Describe the morphology of the erythrocytes.
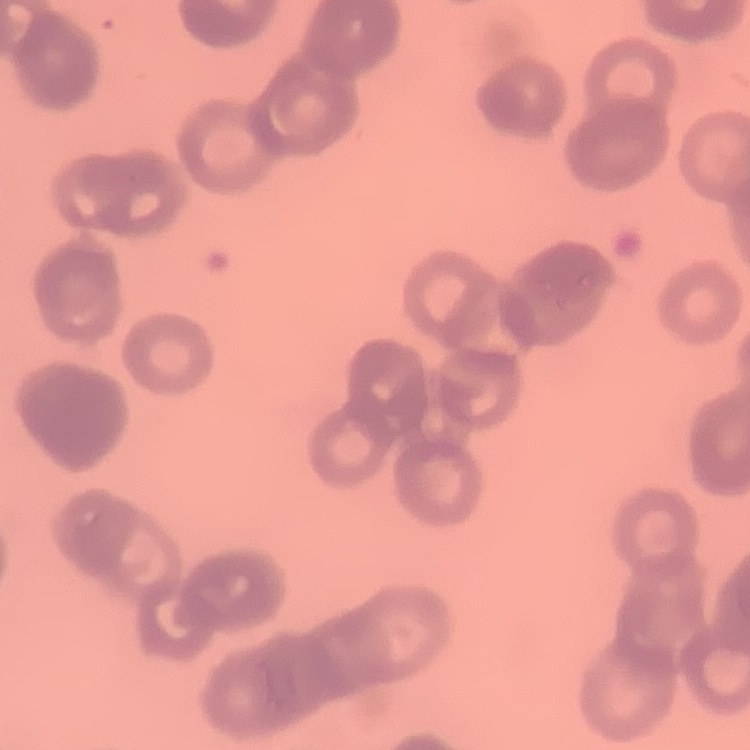

They show rouleaux formation.

Thin peripheral smear. Square crop of a larger photomicrograph. Field's or Giemsa stain.